Mark where platelets are.
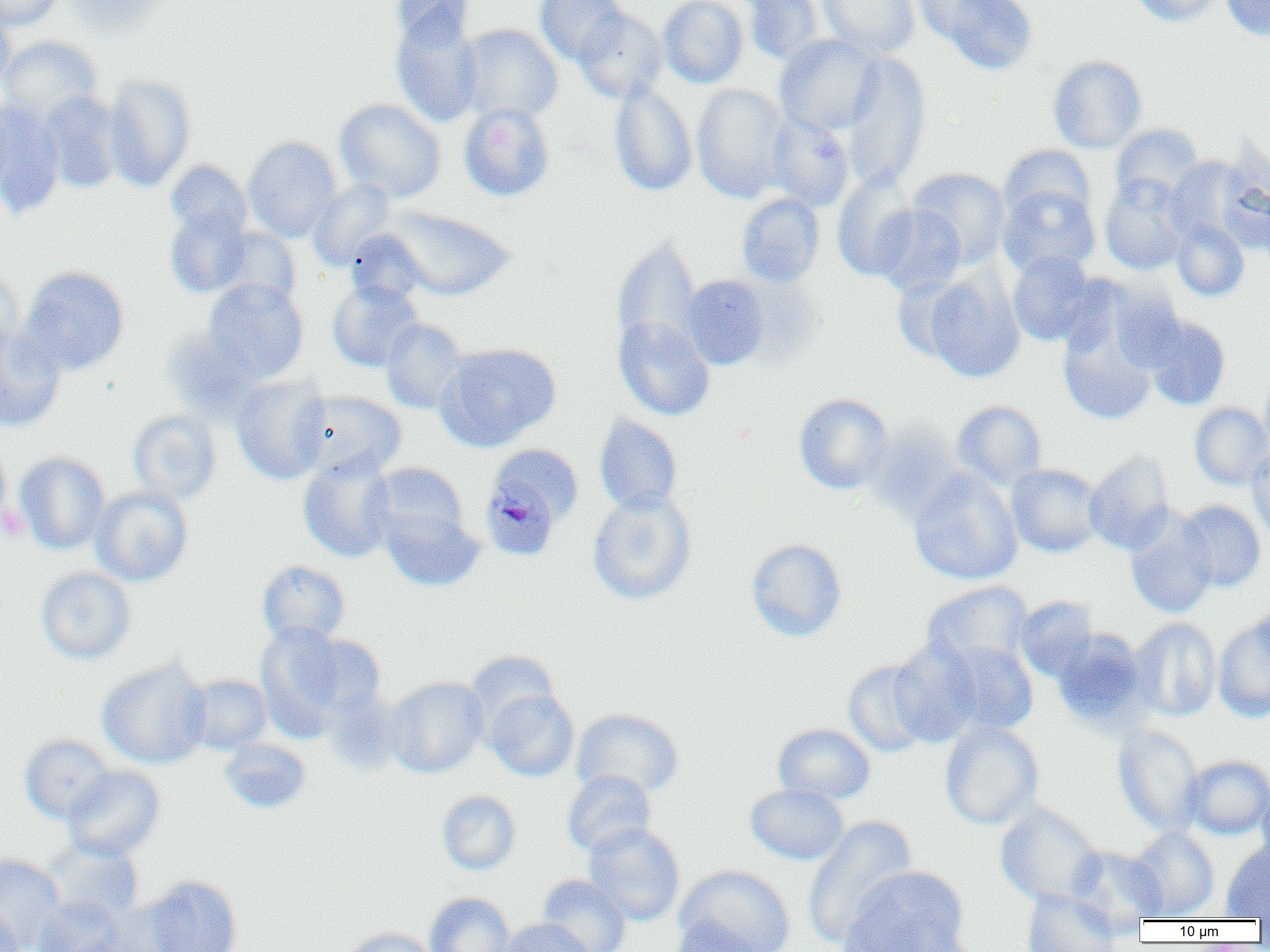

Approximate bounding boxes as (x1,y1)-(x2,y2) corner pairs in pixels.
Platelets: (0,504)-(30,541).

Summary:
  - Uninfected red blood cell locations: (0,0)-(62,29), (63,0)-(168,35), (390,0)-(474,49), (535,0)-(629,66), (658,0)-(749,87), (743,0)-(825,66), (819,0)-(920,57), (910,0)-(1005,42), (939,0)-(1037,74), (1132,0)-(1225,26), (1220,0)-(1270,41), (573,8)-(666,103), (0,9)-(15,90), (390,10)-(484,127), (458,24)-(563,124), (774,34)-(884,135), (0,36)-(103,122), (839,52)-(932,191), (1048,55)-(1147,154), (103,74)-(196,191), (608,80)-(698,197), (691,84)-(791,202), (39,93)-(122,193), (0,96)-(15,200), (334,99)-(446,204), (0,102)-(65,218), (459,103)-(555,201), (766,114)-(854,212), (1111,123)-(1203,205), (243,136)-(342,242), (999,145)-(1095,225), (1164,155)-(1249,245), (165,160)-(252,240), (908,167)-(1011,268), (832,168)-(920,281), (1100,175)-(1192,275), (308,179)-(396,271), (998,184)-(1099,278), (736,193)-(825,287), (873,205)-(966,296), (164,206)-(251,298), (385,207)-(514,301), (1171,220)-(1249,301), (214,227)-(301,308), (345,229)-(429,305), (611,239)-(703,357), (1008,251)-(1100,346), (19,265)-(130,376), (0,268)-(23,362), (922,270)-(1025,382), (681,275)-(770,370), (203,278)-(308,381), (327,280)-(423,372), (1056,296)-(1166,427), (1142,315)-(1231,410), (614,316)-(715,420), (380,318)-(468,414), (0,326)-(66,433), (162,326)-(262,422), (438,343)-(561,450), (1260,371)-(1270,460), (231,375)-(332,484), (297,391)-(407,479), (793,393)-(894,494), (953,401)-(1047,490), (1190,402)-(1270,490), (127,409)-(222,505), (593,415)-(683,515), (862,421)-(965,522), (0,437)-(10,529), (1247,446)-(1270,542), (14,452)-(110,554), (1084,452)-(1175,554), (298,453)-(396,562), (370,462)-(468,545), (1006,464)-(1103,557), (908,468)-(1023,585), (91,485)-(193,587), (587,491)-(697,605), (1176,500)-(1266,592), (380,506)-(484,592), (1125,510)-(1217,619), (746,538)-(847,642), (257,560)-(350,645), (36,567)-(136,664), (922,581)-(1033,671), (1014,596)-(1099,681), (1251,602)-(1270,673), (1213,614)-(1270,722), (1130,618)-(1221,721), (254,623)-(370,736), (1052,629)-(1153,731), (888,637)-(983,748), (941,641)-(1038,736), (464,650)-(560,732), (97,657)-(212,769), (842,659)-(933,757), (183,674)-(271,753), (384,676)-(488,778), (484,688)-(579,781), (571,708)-(684,799), (939,720)-(1043,830), (773,723)-(876,803), (1113,724)-(1205,836), (20,734)-(115,823), (219,738)-(311,814), (1182,755)-(1270,839), (62,765)-(165,861), (562,769)-(656,859), (1255,777)-(1270,871), (744,784)-(850,865), (437,790)-(520,875), (994,801)-(1104,908), (802,815)-(917,948), (583,822)-(685,926), (1127,827)-(1220,920), (42,839)-(144,923), (1221,841)-(1270,919), (1068,846)-(1168,929), (0,853)-(66,950), (675,865)-(796,952), (839,866)-(970,952), (537,874)-(631,952), (139,875)-(243,952), (1022,889)-(1120,952), (424,892)-(515,952), (32,897)-(128,952), (0,900)-(24,952), (667,916)-(767,952), (498,917)-(594,952), (339,927)-(440,952)
  - Plasmodium malariae-infected red blood cell locations: (486,482)-(554,560)
  - Slide-level diagnosis: Plasmodium malariae
  - Image size: 1270×952 pixels
  - Magnification: 1000x
  - Preparation: thin blood smear
  - Modality: optical microscopy
  - Field of view: single